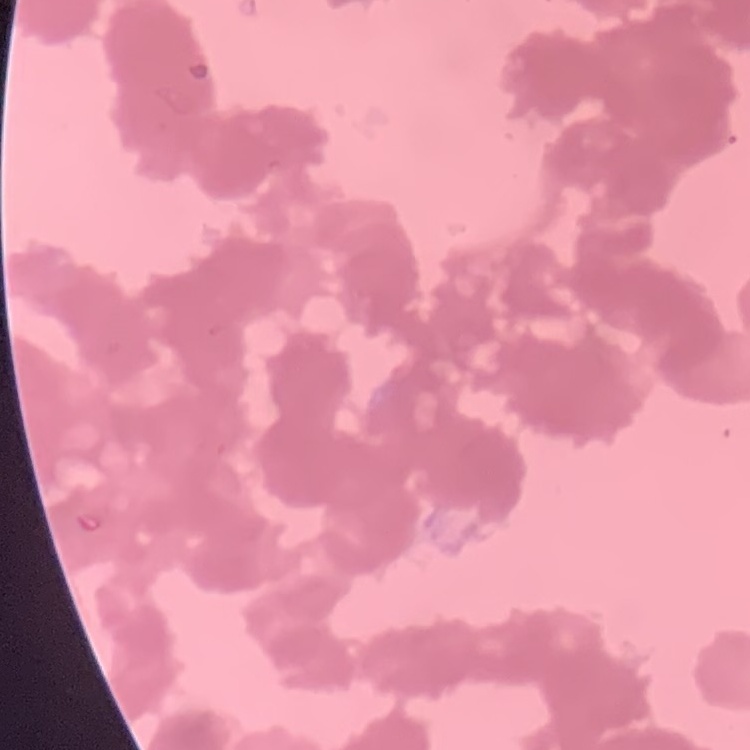
Summary:
  - Red blood cell morphology: rouleaux formation
  - Image type: square crop of a larger photomicrograph
  - Preparation: thin blood smear
  - Stain: Field's or Giemsa